Evaluate for malaria.
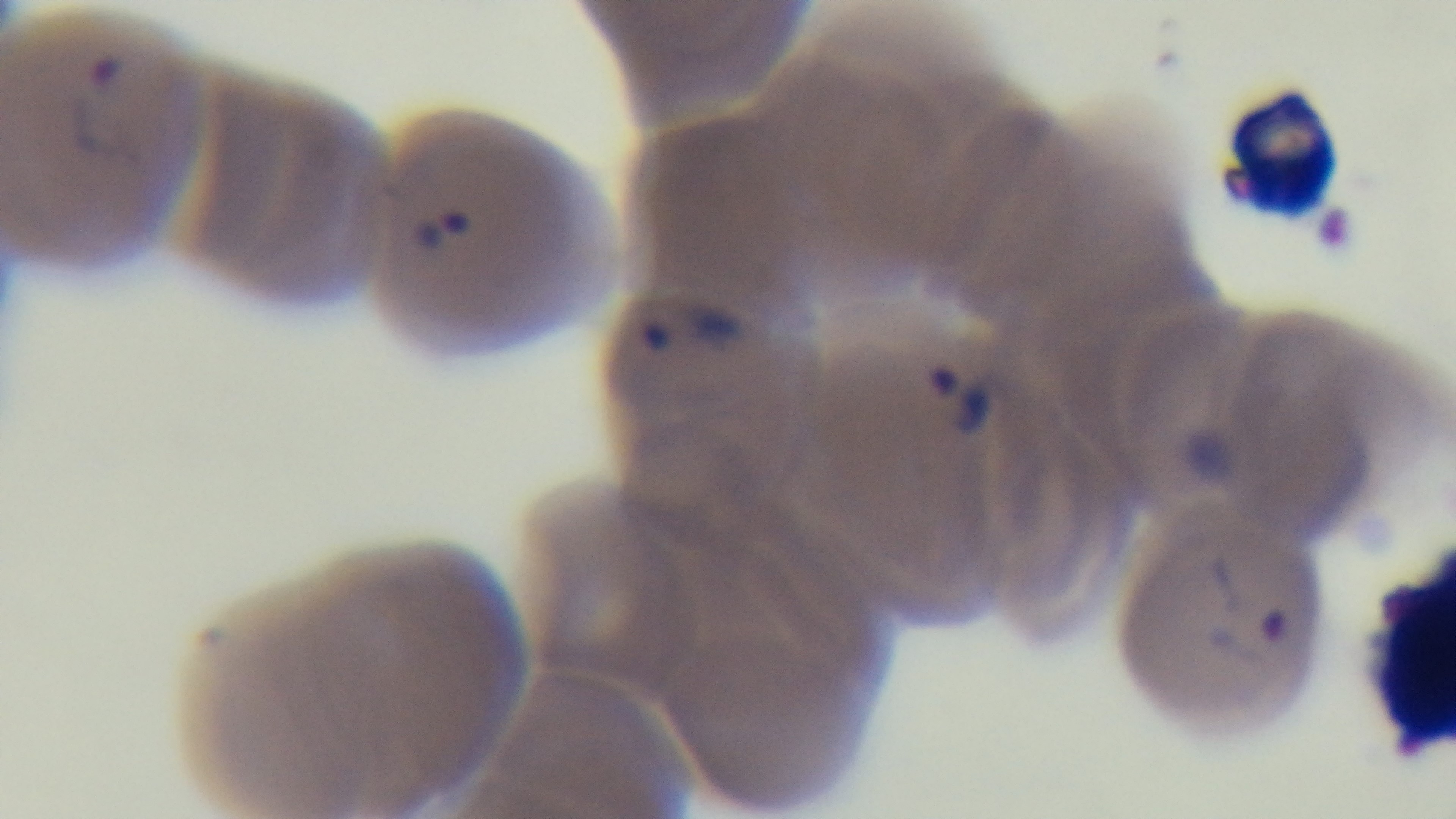
It is infected.

modality = light microscopy
field of view = one from the slide
preparation = thin smear
capture = mounted 4K digital camera
stain = Giemsa
objective = 100x oil immersion